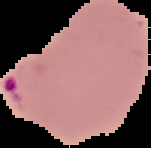

Summary:
  - Result: malaria parasites identified
  - Image size: 151×148 pixels
  - Image type: segmented cell region on a black background
  - Preparation: thin blood film